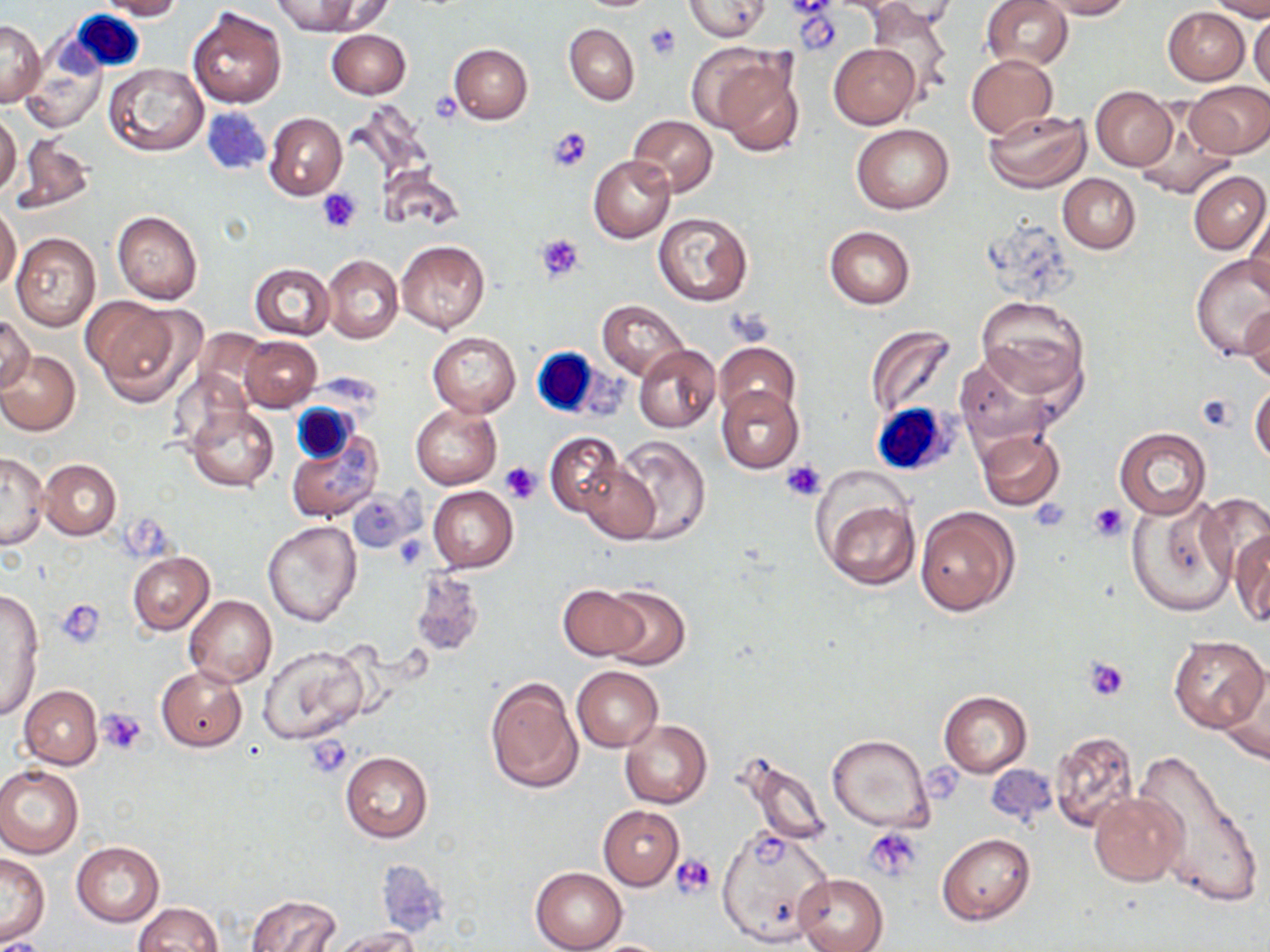
Approximate bounding boxes as [x1, y1, x2, y2] in pixels. Uninfected red blood cell locations: [96, 0, 183, 19], [271, 0, 369, 35], [683, 0, 770, 40], [982, 0, 1074, 71], [1039, 0, 1132, 19], [1209, 0, 1270, 20], [315, 1, 395, 35], [867, 4, 951, 94], [187, 6, 287, 108], [1163, 6, 1250, 84], [1249, 12, 1270, 92], [1, 19, 44, 106], [564, 23, 639, 105], [326, 29, 410, 99], [829, 43, 921, 128], [450, 44, 531, 123], [702, 46, 803, 156], [20, 54, 102, 129], [966, 54, 1058, 139], [102, 62, 208, 156], [1184, 81, 1269, 158], [1090, 86, 1177, 170], [983, 109, 1092, 193], [1132, 111, 1237, 201], [0, 112, 21, 196], [265, 112, 347, 199], [627, 115, 718, 197], [851, 123, 954, 214], [15, 135, 94, 214], [588, 154, 675, 242], [377, 164, 466, 235], [1188, 170, 1268, 254], [1059, 173, 1140, 253], [0, 204, 21, 293], [112, 209, 202, 305], [1244, 211, 1269, 300], [654, 212, 753, 306], [825, 226, 916, 308], [11, 232, 101, 332], [396, 239, 489, 332], [414, 247, 507, 399], [322, 254, 403, 344], [1192, 256, 1270, 361], [248, 263, 333, 340], [976, 297, 1090, 399], [86, 299, 197, 405], [597, 299, 688, 380], [1240, 306, 1270, 383], [0, 316, 32, 394], [865, 324, 957, 419], [192, 331, 272, 407], [427, 332, 520, 416], [240, 336, 322, 411], [713, 342, 801, 421], [634, 344, 720, 433], [0, 351, 81, 436], [954, 353, 1057, 448], [1250, 382, 1270, 466], [716, 387, 804, 473], [411, 404, 501, 490], [421, 405, 507, 573], [186, 406, 279, 492], [1115, 426, 1212, 519], [977, 429, 1064, 510], [287, 430, 381, 521], [546, 433, 622, 516], [611, 435, 712, 545], [1, 452, 48, 550], [40, 459, 120, 540], [578, 459, 659, 544], [428, 486, 517, 572], [1196, 490, 1270, 589], [819, 493, 921, 589], [1127, 496, 1239, 615], [915, 507, 1019, 616], [261, 521, 362, 628], [1231, 527, 1270, 626], [126, 551, 214, 635], [559, 584, 646, 661], [599, 585, 691, 671], [0, 589, 44, 721], [184, 594, 276, 687], [1167, 635, 1268, 732], [258, 645, 369, 744], [1214, 663, 1270, 767], [156, 664, 249, 752], [572, 666, 662, 751], [484, 675, 583, 795], [19, 685, 101, 769], [938, 690, 1032, 777], [620, 719, 711, 809], [1050, 731, 1142, 834], [826, 734, 933, 833], [1136, 745, 1265, 912], [731, 749, 834, 847], [341, 751, 433, 844], [0, 764, 83, 859], [1089, 791, 1185, 886], [597, 805, 683, 889], [717, 826, 836, 947], [938, 833, 1034, 925], [71, 841, 164, 926], [1, 853, 50, 944], [531, 867, 626, 951], [795, 873, 887, 952], [245, 894, 341, 952], [132, 902, 223, 952], [329, 929, 419, 952], [583, 939, 678, 951]. White blood cell locations: [66, 9, 148, 77], [528, 346, 615, 423], [292, 403, 358, 465], [871, 403, 955, 476]. Platelet locations: [786, 0, 834, 19], [644, 22, 681, 62], [430, 92, 463, 123], [546, 126, 591, 172], [317, 189, 362, 233], [535, 233, 583, 282], [727, 310, 774, 346], [1197, 393, 1237, 432], [782, 459, 827, 501], [499, 461, 542, 505], [1031, 498, 1074, 531], [1087, 502, 1129, 541], [57, 599, 104, 647], [1085, 656, 1131, 701], [97, 709, 149, 754], [305, 735, 353, 777], [863, 829, 922, 880], [673, 854, 717, 899]. Slide-level diagnosis: negative for blood parasites. May-Grünwald-Giemsa-stained preparation. Image is 1270×952 pixels. Optical microscopy. Single field of view. Thin blood smear. 1000x magnification.